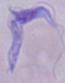

magnification = 1000x
modality = photomicrograph
identification = trypanosome